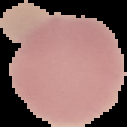
From a thin blood smear. Image is 127×127 pixels. Result: no malaria parasites seen. Segmented cell region on a black background.